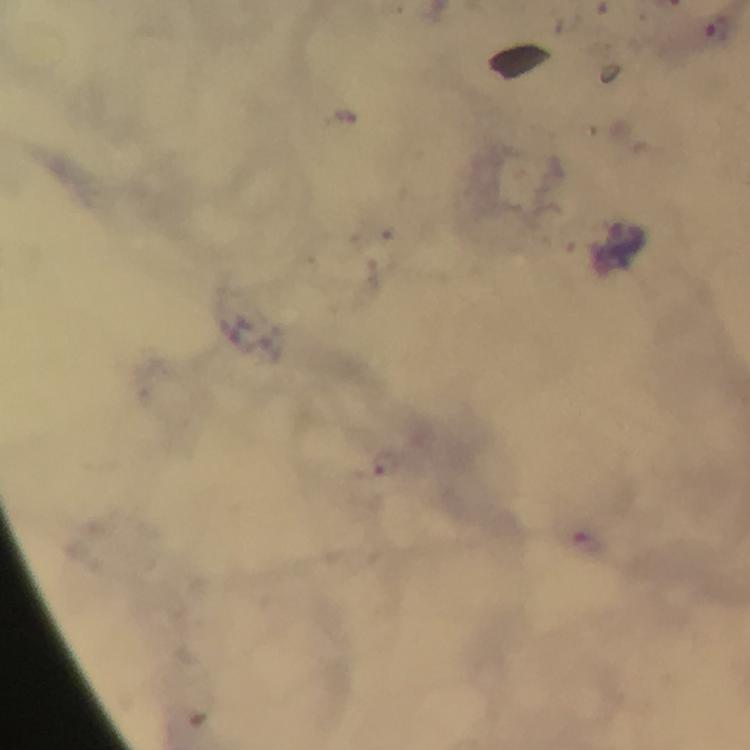
capture = smartphone mounted on the microscope
cropped from = a single field of view
context = from a diagnostic examination for malaria
stain = Giemsa
immersion oil = applied
image size = 750×750 pixels
preparation = thick blood film
magnification = 100x
malaria parasite locations = approximate centers as [x, y] in pixels: [717, 30], [386, 464], [589, 541]